Report the malaria status of this cell.
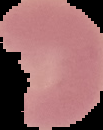

It is parasitized.

image type = segmented cell region on a black background
image size = 103×130 pixels
preparation = thin blood smear